Give the extent of all Plasmodium falciparum-infected red blood cells.
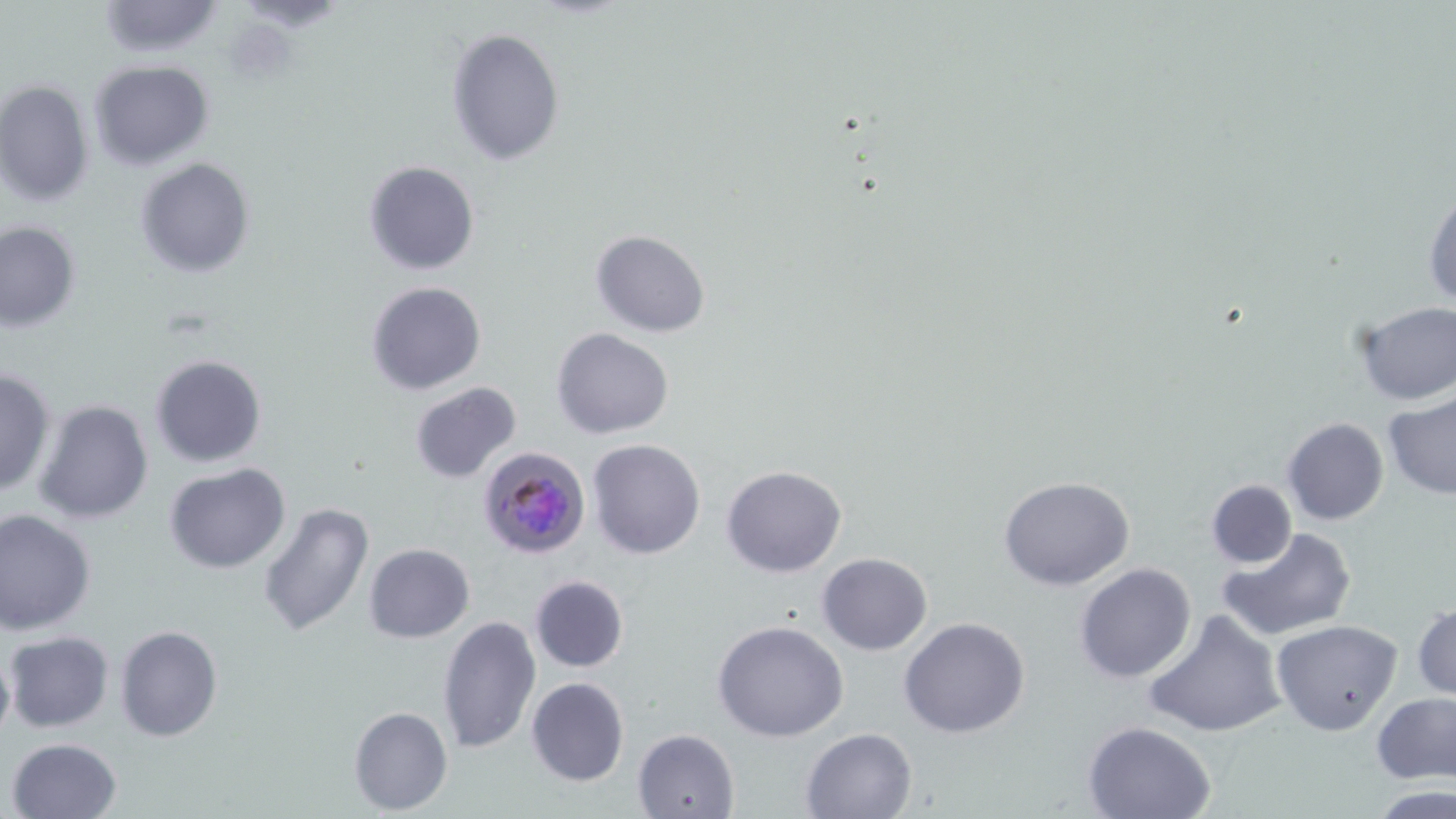

Approximate bounding boxes as (x1, y1, x2, y2) in pixels.
Plasmodium falciparum-infected red blood cells: (478, 445, 592, 559).

Uninfected red blood cell locations: (94, 0, 226, 57), (446, 27, 564, 165), (90, 60, 215, 169), (0, 78, 95, 207), (135, 157, 255, 277), (362, 160, 481, 277), (1423, 180, 1455, 313), (1, 220, 80, 333), (590, 229, 711, 336), (367, 281, 487, 396), (1351, 301, 1456, 406), (552, 328, 674, 440), (150, 354, 268, 468), (0, 368, 55, 497), (410, 382, 523, 484), (1382, 393, 1455, 499), (33, 398, 154, 526), (1282, 417, 1389, 525), (588, 438, 706, 558), (165, 463, 292, 572), (720, 465, 848, 577), (997, 476, 1135, 589), (1205, 479, 1298, 568), (257, 501, 376, 638), (0, 508, 96, 635), (1215, 527, 1357, 642), (364, 542, 475, 642), (816, 553, 933, 655), (1075, 563, 1197, 683), (529, 575, 628, 673), (1412, 600, 1456, 701), (1144, 609, 1287, 739), (437, 615, 542, 754), (900, 616, 1031, 738), (712, 618, 849, 742), (1272, 618, 1401, 735), (115, 625, 223, 743), (4, 630, 114, 734), (0, 641, 14, 749), (525, 677, 630, 787), (1372, 695, 1456, 784), (349, 706, 453, 814), (1082, 721, 1218, 819), (633, 728, 741, 818), (800, 728, 917, 818), (7, 737, 123, 819), (1370, 784, 1456, 818). Slide-level diagnosis: Plasmodium falciparum. Single field of view. Optical microscopy. May-Grünwald-Giemsa stain. Image is 1456×819 pixels. Thin blood smear. 1000x magnification.